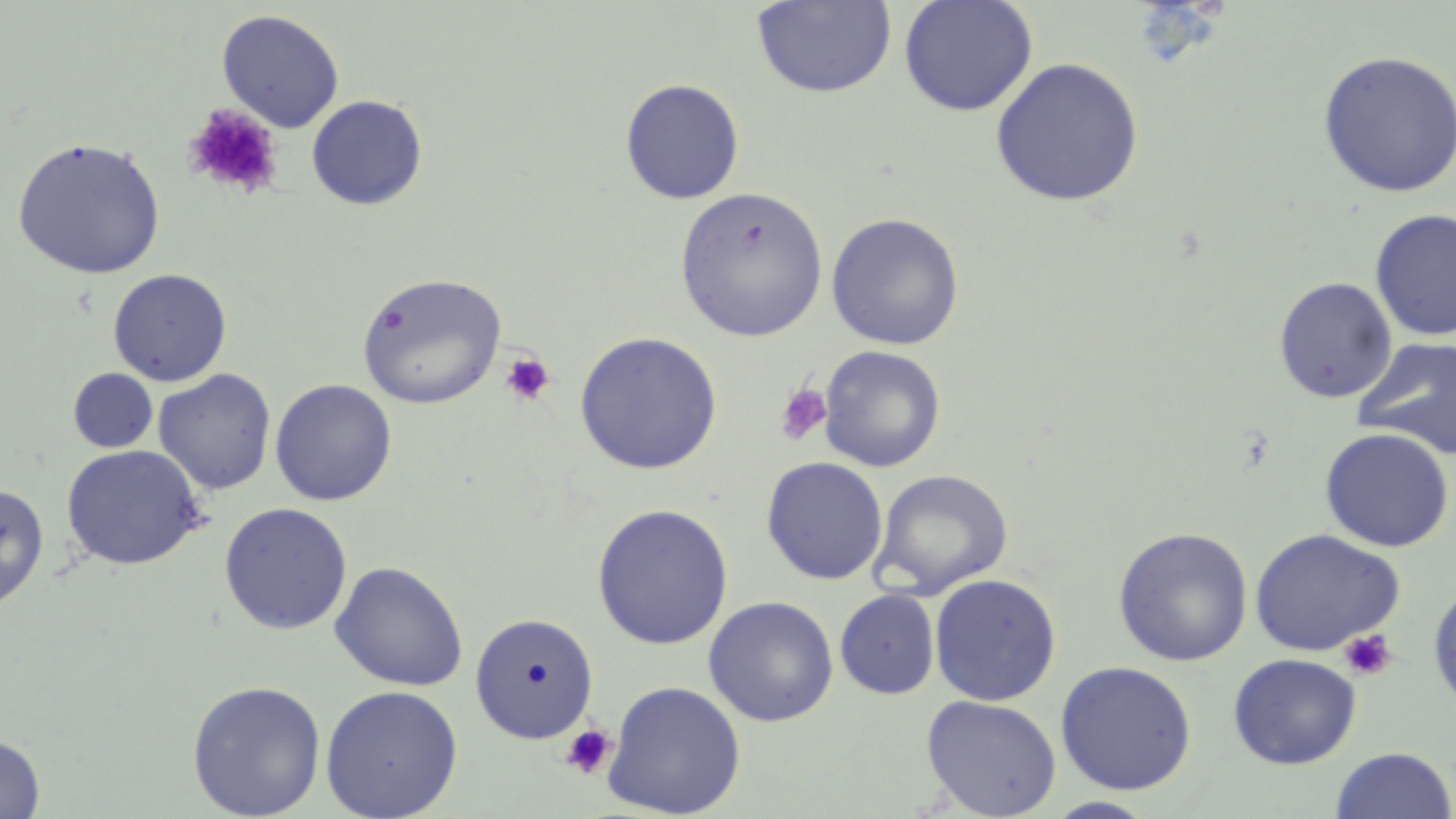

{
  "slide_level_diagnosis": "no evidence of blood parasites",
  "modality": "optical microscopy",
  "uninfected_red_blood_cell_locations": "approximate bounding boxes as (x1,y1)-(x2,y2) corner pairs in pixels: (752,0)-(896,99), (898,0)-(1038,117), (216,9)-(345,132), (1317,50)-(1456,197), (991,57)-(1144,206), (620,78)-(745,204), (306,95)-(428,210), (11,136)-(166,280), (675,186)-(828,342), (1370,209)-(1456,342), (826,212)-(964,350), (108,268)-(232,387), (357,272)-(507,409), (1273,276)-(1398,404), (573,331)-(724,475), (1353,336)-(1456,460), (819,345)-(945,473), (68,368)-(158,453), (153,369)-(276,495), (270,378)-(398,506), (1319,427)-(1454,552), (60,443)-(207,571), (761,457)-(888,585), (872,468)-(1013,597), (0,483)-(50,612), (219,502)-(353,635), (591,503)-(733,650), (1113,527)-(1253,667), (1249,528)-(1405,657), (330,560)-(468,691), (929,573)-(1062,707), (1427,583)-(1456,714), (835,589)-(940,700), (703,596)-(838,727), (469,612)-(600,744), (1228,653)-(1361,770), (1055,661)-(1197,795), (186,679)-(327,819), (603,679)-(746,818), (320,684)-(464,819), (921,695)-(1062,817), (0,733)-(45,818), (1329,747)-(1456,819)",
  "platelet_locations": "approximate bounding boxes as (x1,y1)-(x2,y2) corner pairs in pixels: (185,103)-(283,199), (499,352)-(556,407), (774,383)-(832,446), (1338,628)-(1397,682), (559,724)-(617,779)",
  "magnification": "1000x",
  "stain": "May-Grünwald-Giemsa",
  "field_of_view": "one of a larger specimen",
  "preparation": "thin blood film",
  "image_size": "1456×819 pixels"
}